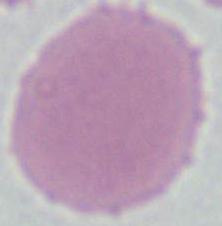

{
  "magnification": "1000x",
  "modality": "micrograph",
  "identification": "red blood cell"
}